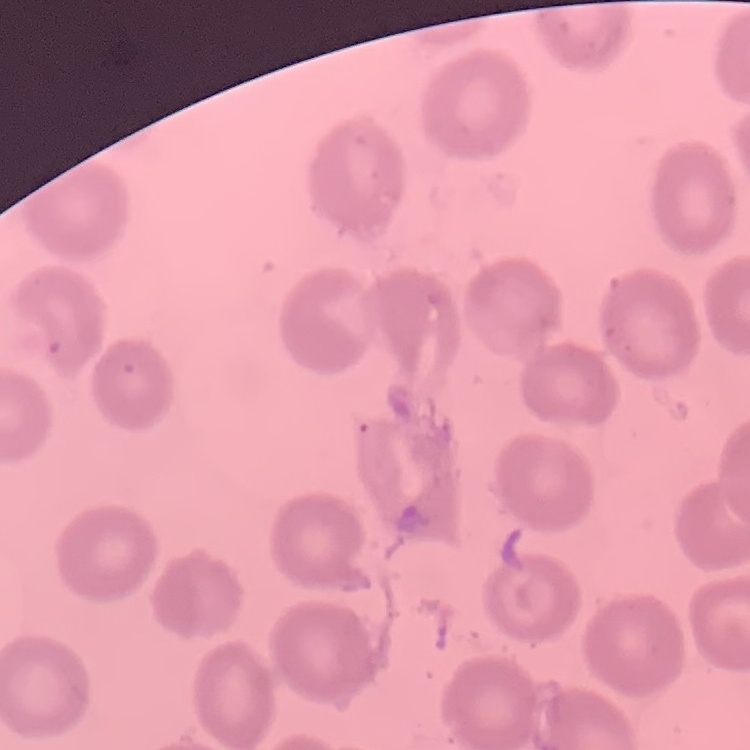

Summary:
  - Erythrocyte morphology: no rouleaux formation
  - Stain: Field's or Giemsa
  - Image type: square crop of a larger photomicrograph
  - Preparation: thin peripheral smear